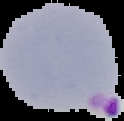

Summary:
  - Image size: 124×121 pixels
  - Preparation: thin blood smear
  - Malaria status: parasitized
  - Image type: segmented cell region with the area outside set to black